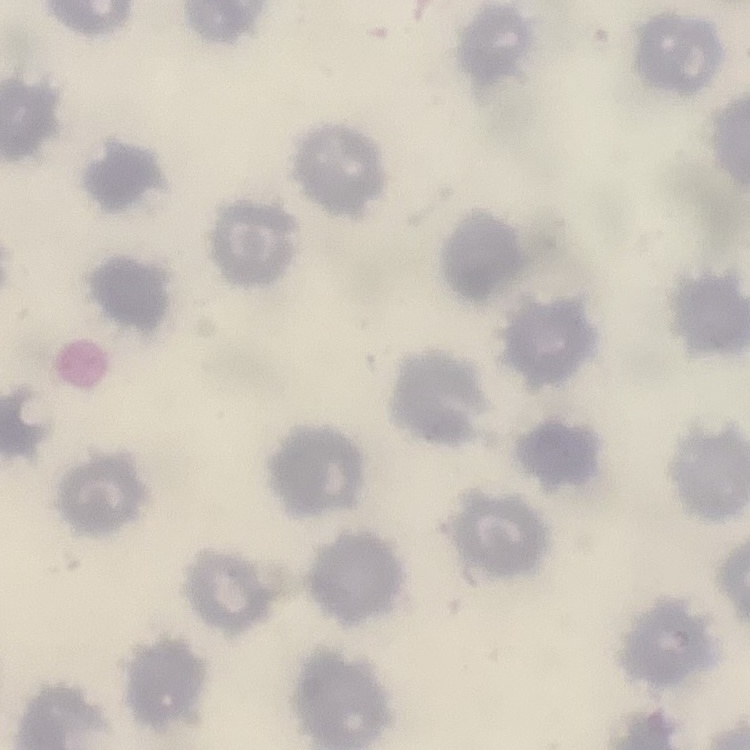

Summary:
  - Red blood cell morphology: no rouleaux formation
  - Image type: one tile cut from a larger photomicrograph
  - Preparation: thin blood smear
  - Stain: Field's or Giemsa